State which parasite is depicted.
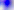

This is Toxoplasma gondii.

magnification = 400x
modality = micrograph